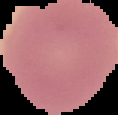

image type = segmented cell region with the area outside set to black
image size = 118×115 pixels
result = no malaria parasites detected
preparation = thin blood smear